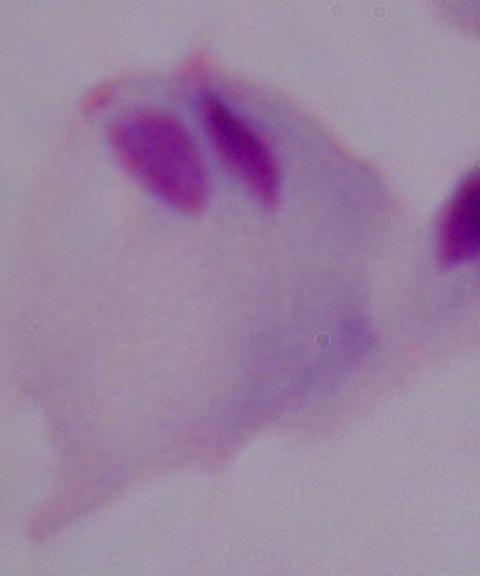
{
  "identification": "trichomonad",
  "modality": "micrograph",
  "magnification": "1000x"
}